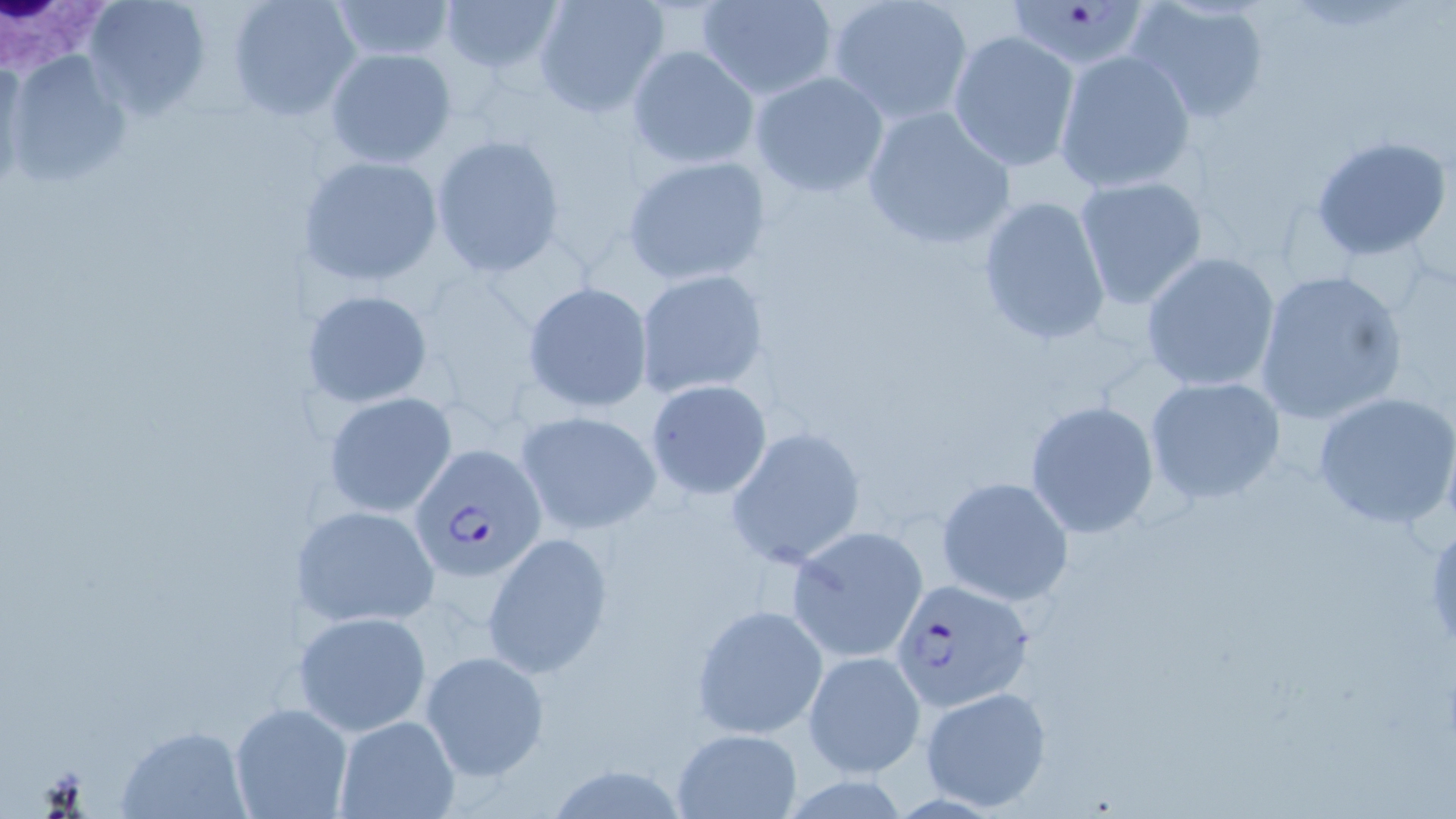
Summary:
  - Coordinate format: approximate bounding boxes as (x1,y1)-(x2,y2) corner pairs in pixels
  - Uninfected red blood cell locations: (83,0)-(212,118), (226,0)-(361,121), (440,0)-(562,77), (696,0)-(839,101), (824,0)-(974,126), (1126,0)-(1273,125), (325,1)-(459,63), (532,1)-(669,118), (948,30)-(1081,173), (627,45)-(759,169), (323,47)-(455,168), (1053,49)-(1197,195), (4,50)-(133,190), (1,60)-(30,189), (749,71)-(890,199), (860,105)-(1017,251), (431,133)-(569,279), (1310,135)-(1452,262), (620,154)-(772,287), (299,155)-(444,287), (1074,176)-(1208,308), (976,195)-(1112,347), (1140,251)-(1281,393), (1253,268)-(1410,426), (633,269)-(769,398), (521,281)-(654,413), (301,288)-(434,409), (1143,376)-(1287,505), (642,379)-(773,499), (1312,389)-(1456,529), (322,392)-(459,517), (1025,400)-(1161,541), (514,409)-(663,536), (725,425)-(866,572), (937,476)-(1073,606), (294,502)-(440,629), (788,527)-(928,661), (481,531)-(613,676), (692,602)-(828,739), (294,611)-(433,735), (419,651)-(548,779), (802,652)-(926,778), (920,685)-(1052,810), (230,702)-(352,819), (333,715)-(459,819), (117,727)-(252,816), (671,728)-(802,818)
  - White blood cell locations: (1,2)-(115,86)
  - Plasmodium falciparum-infected red blood cell locations: (1003,3)-(1155,70), (409,444)-(545,582), (889,578)-(1034,714)
  - Slide-level diagnosis: Plasmodium falciparum
  - Preparation: thin blood smear
  - Stain: May-Grünwald-Giemsa
  - Magnification: 1000x
  - Modality: light microscopy
  - Image size: 1456×819 pixels
  - Field of view: single